Outline each blood parasite and name the species.
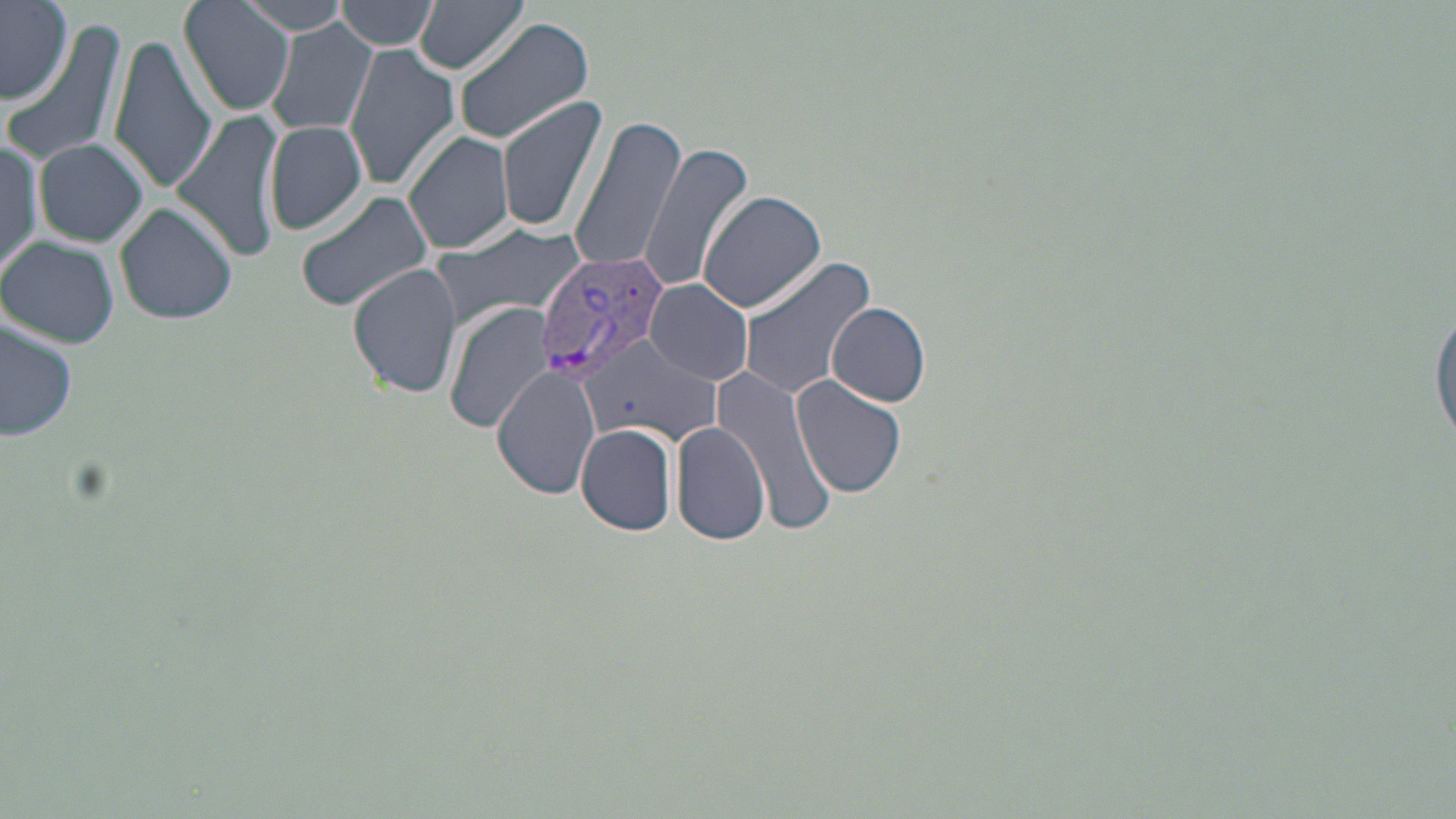

Approximate bounding boxes as [x1, y1, x2, y2] in pixels.
Plasmodium vivax-infected red blood cells: [537, 246, 667, 381].
No Plasmodium falciparum, Plasmodium ovale, Plasmodium malariae, Babesia divergens, or Trypanosoma brucei observed.

slide-level diagnosis = Plasmodium vivax
field of view = single
preparation = thin blood film
stain = May-Grünwald-Giemsa
image size = 1456×819 pixels
uninfected red blood cell locations = approximate bounding boxes as [x1, y1, x2, y2] in pixels: [178, 0, 293, 117], [238, 0, 361, 33], [334, 0, 441, 52], [413, 0, 529, 76], [0, 1, 74, 105], [452, 18, 596, 145], [3, 19, 130, 168], [267, 21, 377, 140], [109, 37, 217, 192], [342, 45, 460, 192], [497, 93, 610, 234], [174, 108, 288, 261], [568, 114, 688, 276], [262, 120, 369, 235], [404, 129, 514, 255], [35, 139, 149, 247], [0, 140, 41, 278], [638, 141, 755, 294], [699, 189, 826, 314], [296, 190, 435, 313], [113, 200, 238, 325], [429, 223, 590, 331], [0, 235, 119, 348], [736, 256, 877, 401], [349, 263, 463, 399], [645, 280, 755, 386], [1430, 289, 1456, 460], [826, 301, 931, 406], [443, 302, 555, 432], [0, 318, 78, 446], [582, 333, 721, 446], [705, 360, 839, 534], [494, 366, 601, 499], [791, 374, 907, 499], [670, 421, 769, 546], [575, 423, 678, 535]
modality = optical microscopy
magnification = 1000x